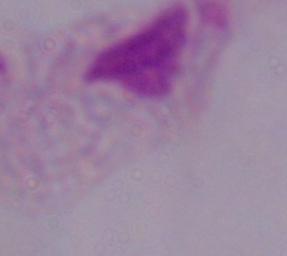

Summary:
  - Modality: photomicrograph
  - Identification: trichomonad
  - Magnification: 1000x